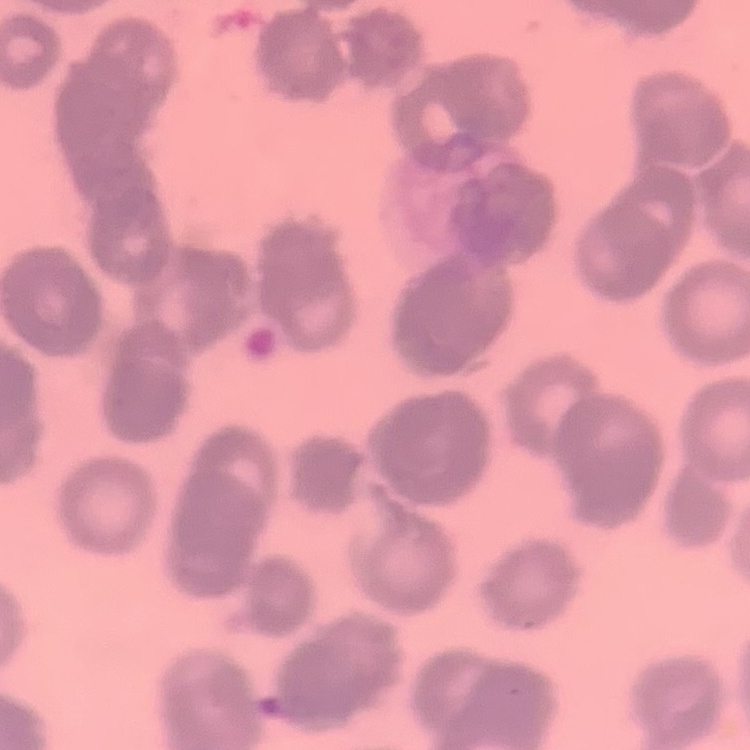
Summary:
  - Erythrocyte morphology: rouleaux formation
  - Stain: Field's or Giemsa
  - Preparation: thin peripheral smear
  - Image type: one tile cut from a larger photomicrograph